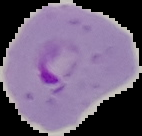

Malaria status: parasitized. Segmented cell region on a black background. Image is 142×136 pixels. From a thin blood smear.